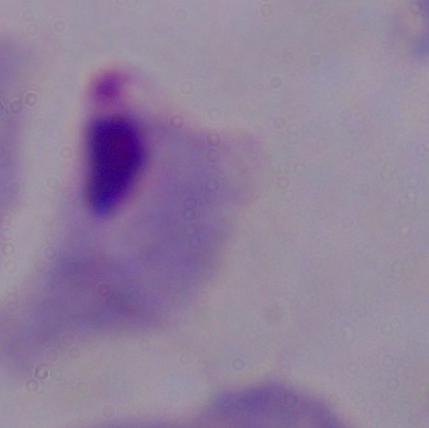

Summary:
  - Magnification: 1000x
  - Identification: trichomonad
  - Modality: micrograph